Assess this cell for malaria.
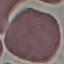
It is uninfected.

Summary:
  - Image type: cell patch, automatically extracted from a larger field of view and resized to 64 × 64 pixels
  - Stain: Giemsa
  - Capture: smartphone through the microscope eyepiece
  - Preparation: thin smear